Outline each blood parasite and name the species.
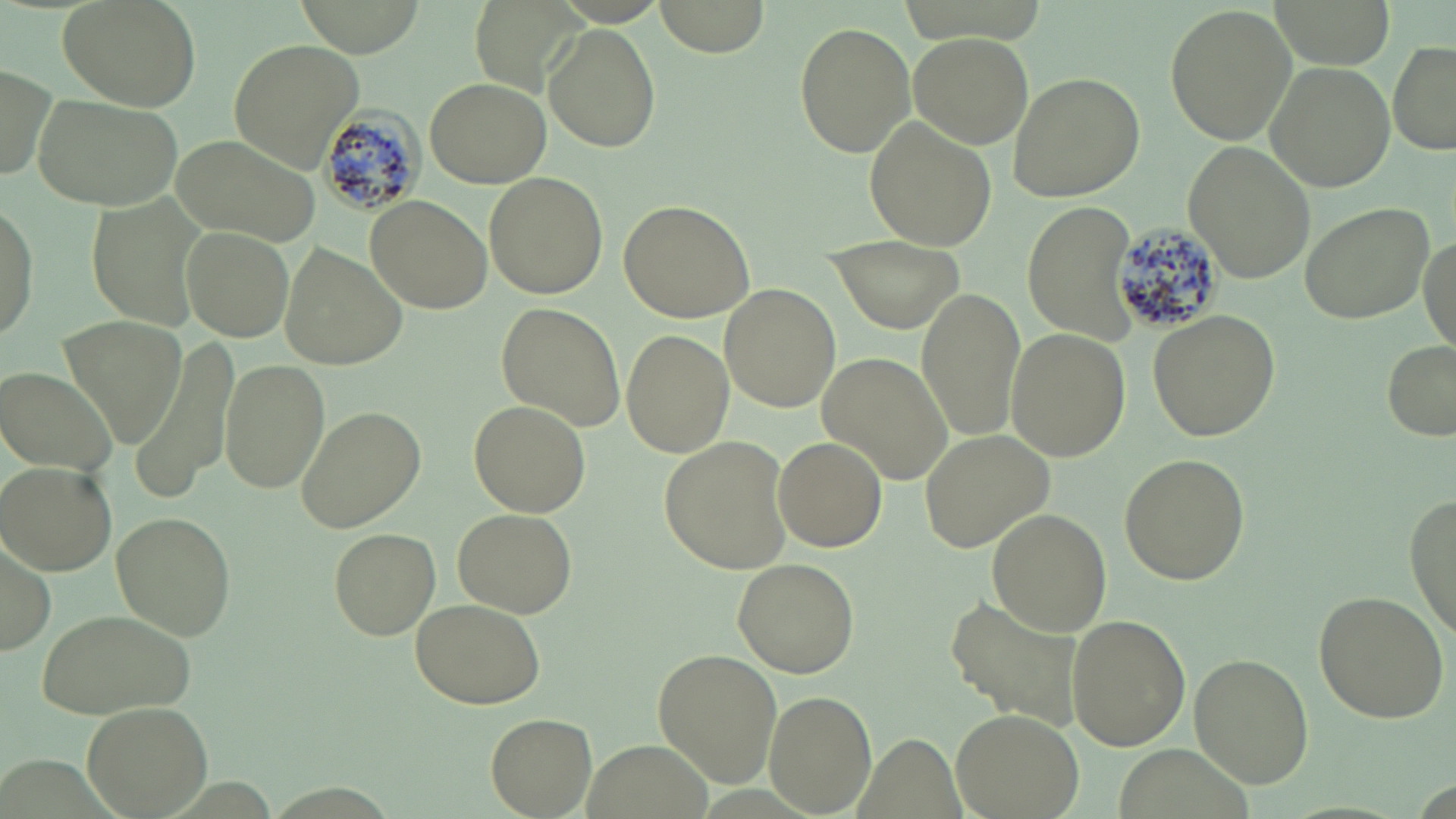

Approximate bounding boxes as (x1, y1, x2, y2) in pixels.
Plasmodium malariae-infected red blood cells: (322, 103, 429, 219), (1110, 216, 1222, 339).
No Plasmodium falciparum, Plasmodium ovale, Plasmodium vivax, Babesia divergens, or Trypanosoma brucei observed.

Summary:
  - Uninfected red blood cell locations: (57, 0, 201, 111), (648, 0, 773, 57), (1165, 4, 1295, 146), (793, 21, 917, 158), (543, 26, 660, 153), (908, 32, 1033, 147), (229, 37, 366, 170), (1388, 41, 1455, 156), (1265, 61, 1394, 189), (0, 64, 57, 185), (1005, 72, 1144, 202), (425, 75, 550, 187), (27, 91, 184, 213), (866, 117, 996, 251), (167, 135, 318, 246), (1182, 138, 1318, 284), (484, 171, 609, 299), (366, 195, 490, 314), (619, 199, 754, 323), (1299, 199, 1435, 325), (1026, 200, 1138, 344), (0, 201, 39, 347), (181, 226, 296, 341), (1418, 231, 1454, 349), (831, 236, 961, 335), (279, 245, 406, 372), (720, 284, 839, 411), (918, 287, 1027, 441), (497, 302, 625, 430), (1147, 310, 1279, 441), (59, 314, 188, 444), (621, 328, 734, 459), (1003, 328, 1129, 462), (136, 336, 238, 496), (1383, 340, 1456, 440), (818, 351, 955, 486), (220, 358, 329, 494), (3, 366, 120, 475), (468, 400, 589, 515), (294, 405, 426, 535), (921, 429, 1059, 553), (659, 436, 794, 575), (774, 437, 886, 551), (1120, 453, 1249, 585), (2, 463, 117, 575), (1405, 494, 1456, 634), (452, 507, 578, 619), (986, 509, 1111, 636), (111, 512, 234, 639), (2, 527, 56, 658), (329, 528, 441, 639), (733, 558, 858, 678), (1312, 589, 1450, 724), (409, 598, 546, 710), (946, 598, 1084, 729), (34, 607, 196, 719), (1066, 614, 1191, 750), (652, 647, 780, 787), (1191, 651, 1313, 788), (765, 689, 875, 812), (82, 700, 214, 818), (950, 707, 1083, 819), (485, 713, 596, 816), (585, 737, 707, 819)
  - Slide-level diagnosis: Plasmodium malariae
  - Preparation: thin blood smear
  - Modality: light microscopy
  - Magnification: 1000x
  - Image size: 1456×819 pixels
  - Field of view: one of a larger specimen
  - Stain: May-Grünwald-Giemsa